Name the blood parasite species.
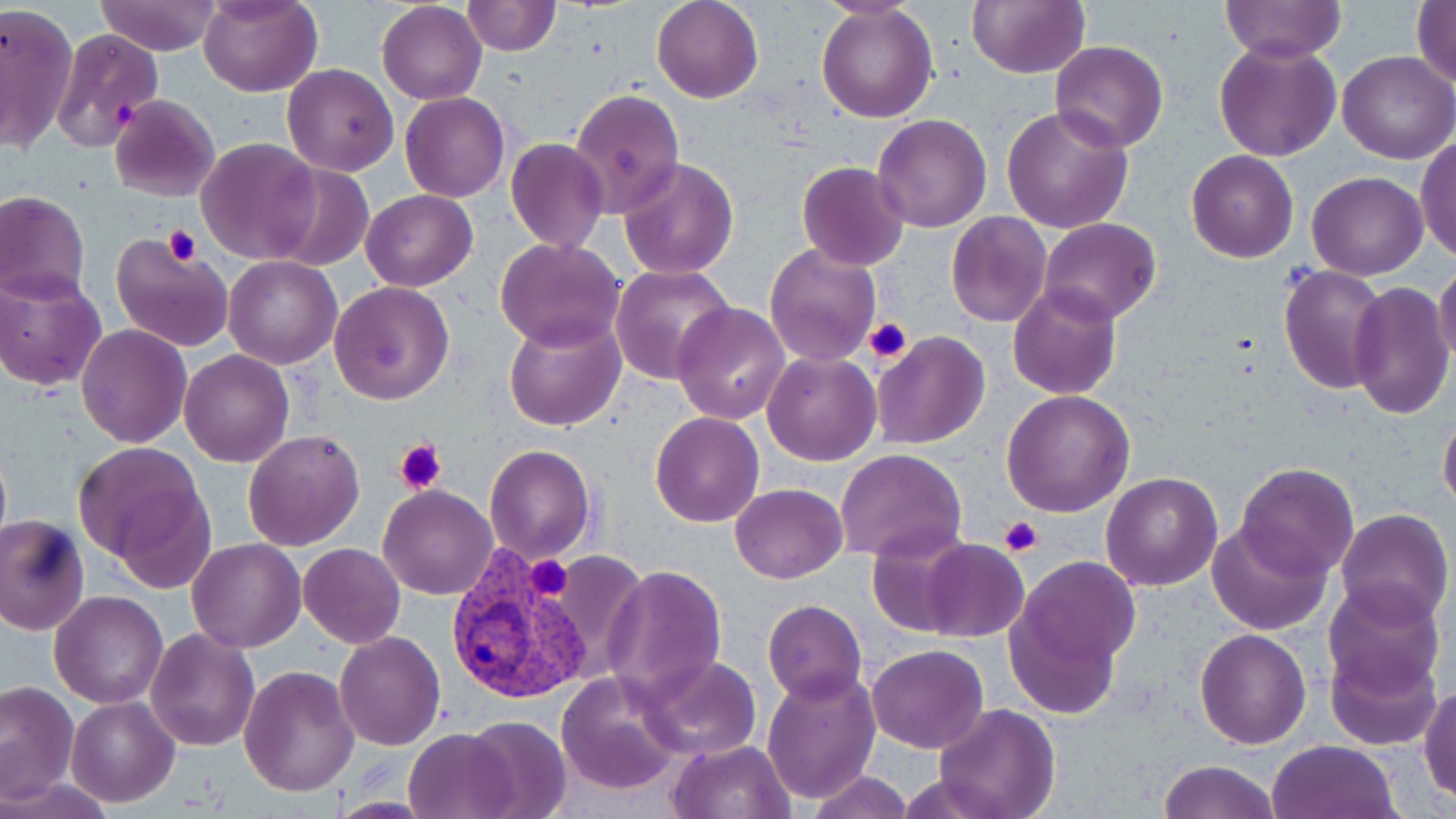
Plasmodium vivax.

Approximate bounding boxes as (x1, y1, x2, y2) in pixels. Platelet locations: (113, 100, 141, 129), (165, 224, 201, 267), (862, 317, 912, 364), (395, 437, 447, 495), (998, 515, 1042, 555), (526, 554, 575, 601). Uninfected red blood cell locations: (94, 0, 223, 56), (200, 0, 322, 98), (652, 0, 762, 103), (966, 0, 1089, 78), (1219, 0, 1346, 64), (1410, 0, 1456, 89), (377, 1, 487, 105), (462, 1, 559, 56), (1, 2, 79, 153), (817, 4, 939, 122), (49, 29, 165, 152), (1213, 39, 1341, 162), (1050, 40, 1168, 152), (1337, 50, 1455, 165), (283, 63, 399, 176), (570, 90, 685, 217), (400, 93, 511, 202), (110, 94, 221, 202), (1002, 104, 1133, 233), (872, 113, 992, 233), (1416, 136, 1456, 264), (197, 138, 321, 264), (506, 138, 609, 255), (1186, 149, 1298, 262), (619, 155, 739, 279), (796, 161, 909, 272), (266, 163, 374, 269), (1306, 170, 1428, 279), (360, 189, 479, 291), (0, 191, 89, 304), (944, 212, 1051, 327), (1039, 217, 1161, 325), (110, 229, 236, 353), (496, 238, 624, 352), (765, 241, 881, 366), (223, 256, 343, 369), (1434, 259, 1456, 370), (610, 263, 737, 387), (1280, 265, 1389, 394), (0, 271, 107, 392), (328, 282, 455, 404), (1348, 282, 1454, 420), (1007, 284, 1122, 400), (672, 303, 791, 424), (504, 314, 625, 432), (75, 325, 192, 447), (870, 331, 990, 450), (179, 350, 294, 467), (762, 351, 881, 465), (1002, 389, 1133, 518), (1438, 405, 1456, 517), (649, 411, 764, 528), (242, 428, 365, 550), (0, 439, 11, 564), (72, 440, 211, 568), (484, 444, 596, 564), (836, 448, 967, 563), (1236, 462, 1360, 578), (1099, 472, 1222, 591), (110, 479, 219, 595), (729, 483, 846, 582), (379, 484, 497, 600), (1334, 507, 1453, 629), (0, 513, 92, 636), (1206, 520, 1331, 635), (867, 528, 980, 636), (188, 538, 306, 654), (918, 538, 1029, 642), (298, 543, 405, 648), (1009, 554, 1142, 691), (603, 564, 727, 702), (1323, 581, 1447, 696), (49, 589, 169, 709), (762, 600, 866, 704), (146, 626, 261, 750), (1195, 628, 1311, 749), (334, 630, 446, 750), (1324, 643, 1442, 752), (866, 644, 989, 753), (638, 653, 761, 762), (277, 656, 443, 776), (239, 665, 359, 796), (761, 669, 882, 804), (557, 670, 683, 797), (0, 680, 78, 804), (1418, 685, 1455, 801), (66, 696, 178, 806), (932, 702, 1060, 819), (464, 714, 572, 817), (405, 729, 515, 817), (669, 738, 797, 819), (1268, 740, 1400, 819), (1158, 760, 1279, 819), (806, 771, 913, 819), (4, 775, 116, 817), (327, 795, 437, 817). Plasmodium vivax-infected red blood cell locations: (449, 550, 593, 703). Image is 1456×819 pixels. 1000x magnification. Light microscopy. Thin blood film. One field of a larger specimen. May-Grünwald-Giemsa stain.